Report the malaria status of this cell.
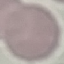
It is uninfected.

Automatically extracted cell patch, resized to 64 × 64 pixels. Thin smear of blood. Acquired by smartphone through the microscope eyepiece. Giemsa stain.